Locate every Plasmodium vivax-infected red blood cell.
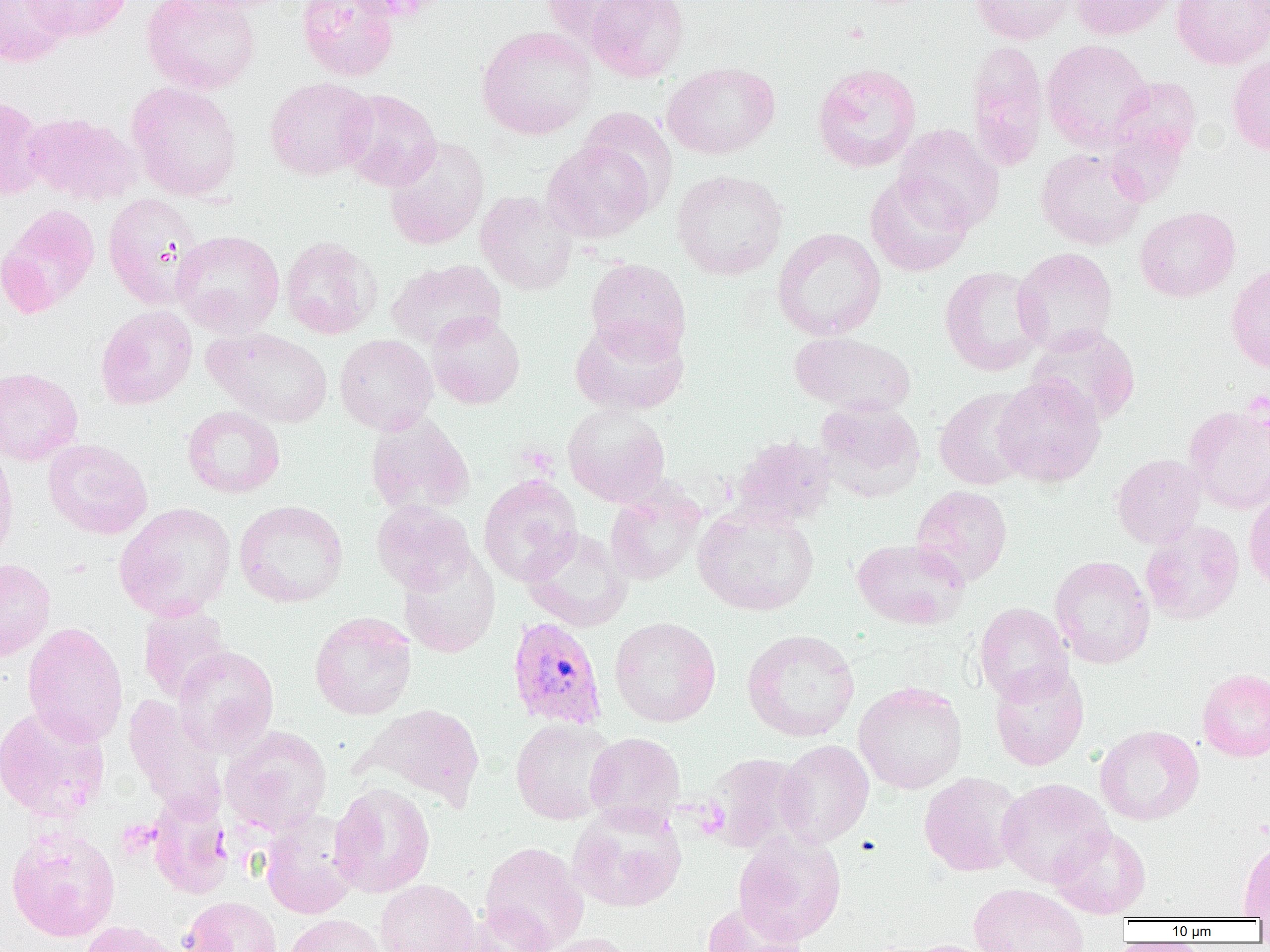
Approximate bounding boxes as named x1/y1/x2/y2 corners in pixels.
Plasmodium vivax-infected red blood cells: (x1=507, y1=616, x2=607, y2=729).

slide-level diagnosis = Plasmodium vivax
image size = 1270×952 pixels
uninfected red blood cell locations = approximate bounding boxes as named x1/y1/x2/y2 corners in pixels: (x1=0, y1=0, x2=72, y2=66), (x1=25, y1=0, x2=131, y2=42), (x1=141, y1=0, x2=260, y2=95), (x1=174, y1=0, x2=297, y2=14), (x1=296, y1=0, x2=400, y2=81), (x1=541, y1=0, x2=653, y2=49), (x1=585, y1=0, x2=689, y2=82), (x1=968, y1=0, x2=1076, y2=44), (x1=1071, y1=0, x2=1176, y2=40), (x1=1171, y1=0, x2=1270, y2=69), (x1=476, y1=25, x2=597, y2=140), (x1=1041, y1=39, x2=1153, y2=151), (x1=965, y1=40, x2=1049, y2=172), (x1=1227, y1=55, x2=1270, y2=157), (x1=661, y1=62, x2=780, y2=159), (x1=812, y1=62, x2=921, y2=173), (x1=264, y1=77, x2=375, y2=180), (x1=1109, y1=77, x2=1201, y2=164), (x1=126, y1=81, x2=242, y2=201), (x1=338, y1=89, x2=442, y2=191), (x1=0, y1=93, x2=48, y2=201), (x1=577, y1=107, x2=678, y2=215), (x1=23, y1=112, x2=142, y2=206), (x1=892, y1=124, x2=1005, y2=233), (x1=1105, y1=125, x2=1188, y2=206), (x1=384, y1=136, x2=489, y2=250), (x1=542, y1=139, x2=656, y2=243), (x1=1036, y1=148, x2=1147, y2=250), (x1=671, y1=169, x2=788, y2=280), (x1=865, y1=172, x2=973, y2=277), (x1=475, y1=191, x2=578, y2=295), (x1=103, y1=193, x2=206, y2=310), (x1=0, y1=203, x2=100, y2=317), (x1=1135, y1=206, x2=1240, y2=302), (x1=772, y1=227, x2=886, y2=341), (x1=171, y1=230, x2=285, y2=337), (x1=280, y1=236, x2=382, y2=339), (x1=1012, y1=247, x2=1118, y2=354), (x1=585, y1=258, x2=691, y2=361), (x1=386, y1=259, x2=506, y2=351), (x1=1226, y1=263, x2=1270, y2=372), (x1=939, y1=266, x2=1047, y2=376), (x1=96, y1=306, x2=197, y2=410), (x1=426, y1=311, x2=525, y2=409), (x1=570, y1=317, x2=689, y2=415), (x1=1027, y1=325, x2=1140, y2=425), (x1=205, y1=326, x2=333, y2=427), (x1=789, y1=331, x2=917, y2=416), (x1=334, y1=334, x2=438, y2=435), (x1=0, y1=366, x2=83, y2=465), (x1=992, y1=374, x2=1106, y2=487), (x1=934, y1=387, x2=1035, y2=490), (x1=814, y1=400, x2=925, y2=501), (x1=563, y1=403, x2=671, y2=507), (x1=1183, y1=404, x2=1270, y2=513), (x1=182, y1=405, x2=285, y2=498), (x1=365, y1=413, x2=475, y2=516), (x1=731, y1=435, x2=837, y2=529), (x1=43, y1=439, x2=153, y2=540), (x1=0, y1=444, x2=17, y2=566), (x1=1112, y1=453, x2=1206, y2=549), (x1=478, y1=474, x2=583, y2=585), (x1=605, y1=483, x2=706, y2=586), (x1=911, y1=485, x2=1013, y2=587), (x1=1244, y1=489, x2=1270, y2=594), (x1=371, y1=499, x2=475, y2=594), (x1=234, y1=500, x2=349, y2=607), (x1=113, y1=502, x2=236, y2=621), (x1=693, y1=505, x2=819, y2=615), (x1=1140, y1=520, x2=1244, y2=625), (x1=520, y1=527, x2=633, y2=631), (x1=851, y1=537, x2=970, y2=630), (x1=398, y1=547, x2=500, y2=658), (x1=1049, y1=555, x2=1155, y2=669), (x1=0, y1=558, x2=55, y2=661), (x1=975, y1=602, x2=1074, y2=706), (x1=138, y1=604, x2=233, y2=703), (x1=309, y1=611, x2=416, y2=720), (x1=610, y1=616, x2=721, y2=726), (x1=22, y1=622, x2=128, y2=747), (x1=742, y1=629, x2=860, y2=742), (x1=173, y1=645, x2=279, y2=757), (x1=989, y1=665, x2=1089, y2=771), (x1=1197, y1=668, x2=1270, y2=762), (x1=854, y1=681, x2=968, y2=794), (x1=124, y1=694, x2=228, y2=822), (x1=357, y1=703, x2=486, y2=811), (x1=0, y1=704, x2=110, y2=823), (x1=510, y1=717, x2=616, y2=825), (x1=220, y1=725, x2=332, y2=835), (x1=1095, y1=725, x2=1204, y2=825), (x1=584, y1=732, x2=685, y2=829), (x1=774, y1=740, x2=874, y2=847), (x1=703, y1=752, x2=808, y2=853), (x1=919, y1=772, x2=1025, y2=876), (x1=996, y1=778, x2=1114, y2=886), (x1=329, y1=782, x2=436, y2=898), (x1=147, y1=797, x2=233, y2=899), (x1=567, y1=803, x2=687, y2=913), (x1=260, y1=811, x2=360, y2=919), (x1=5, y1=825, x2=121, y2=942), (x1=1050, y1=827, x2=1151, y2=918), (x1=733, y1=830, x2=846, y2=944), (x1=1239, y1=838, x2=1270, y2=919), (x1=480, y1=841, x2=589, y2=952), (x1=375, y1=879, x2=478, y2=952), (x1=969, y1=883, x2=1089, y2=952), (x1=181, y1=896, x2=282, y2=952), (x1=701, y1=901, x2=810, y2=951), (x1=457, y1=904, x2=557, y2=952), (x1=285, y1=914, x2=386, y2=952), (x1=75, y1=921, x2=181, y2=952), (x1=539, y1=933, x2=638, y2=952), (x1=904, y1=939, x2=999, y2=952)
preparation = thin blood smear
modality = light microscopy
field of view = one of a larger specimen
magnification = 1000x